Describe the morphology of the erythrocytes.
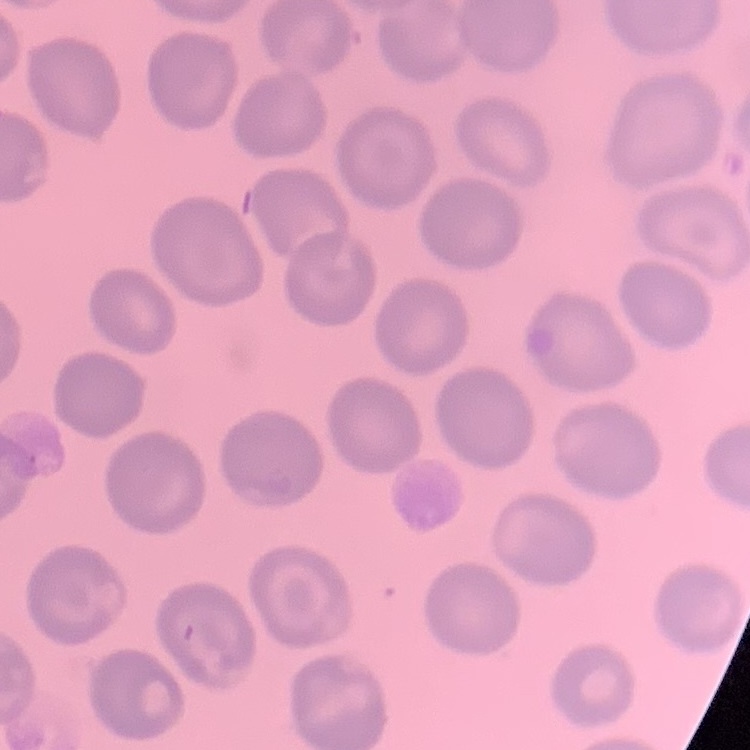
They show no rouleaux formation.

One tile cut from a larger photomicrograph. Field's or Giemsa stain. Thin blood film.